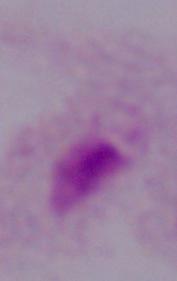
Summary:
  - Magnification: 1000x
  - Modality: micrograph
  - Identification: trichomonad